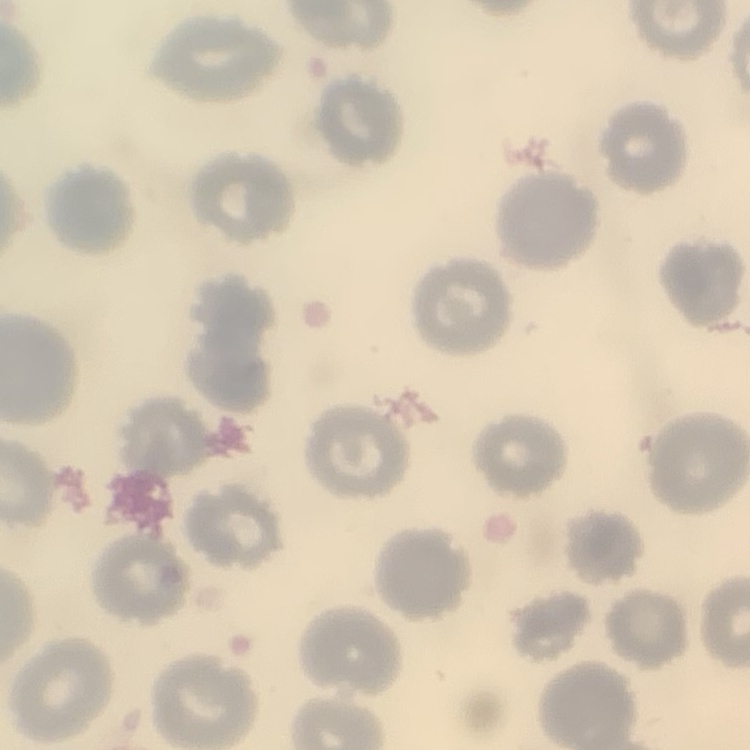

The erythrocytes show no rouleaux formation. Square crop of a larger photomicrograph. Thin peripheral smear. Field's or Giemsa stain.